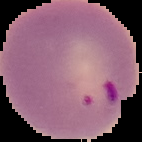

Summary:
  - Result: malaria parasites identified
  - Preparation: thin blood film
  - Image type: segmented cell region with the area outside set to black
  - Image size: 142×142 pixels